Give the extent of all Plasmodium falciparum-infected red blood cells.
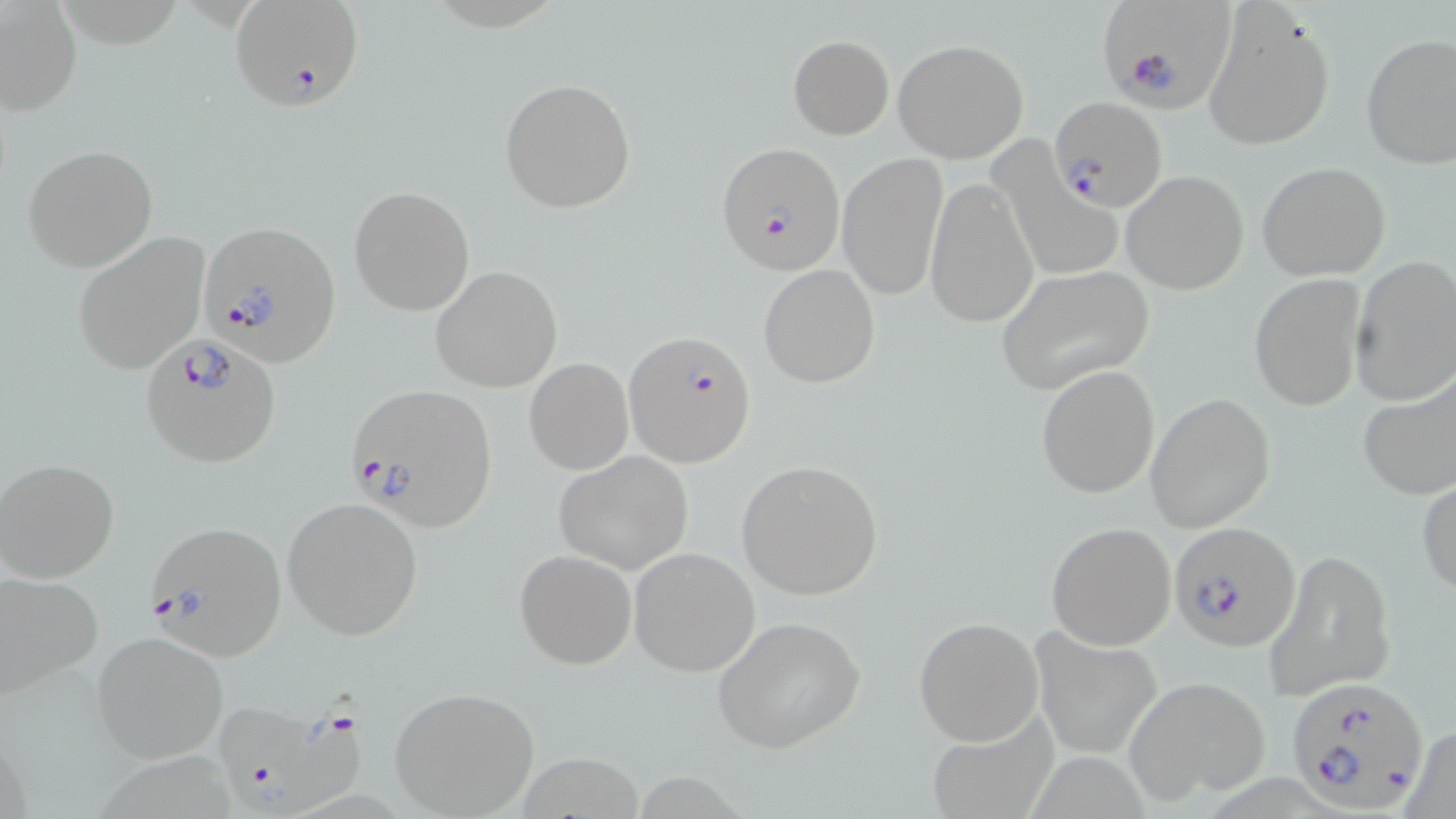
Approximate bounding boxes as (x1,y1)-(x2,y2) corner pairs in pixels.
Plasmodium falciparum-infected red blood cells: (228,1)-(364,113), (1099,2)-(1237,114), (1050,97)-(1166,212), (716,142)-(846,276), (193,229)-(336,362), (625,328)-(757,468), (140,333)-(282,467), (344,382)-(499,533), (141,521)-(285,658), (1168,521)-(1300,653), (1286,677)-(1430,814), (212,692)-(374,818).

{
  "slide_level_diagnosis": "Plasmodium falciparum",
  "preparation": "thin blood film",
  "image_size": "1456×819 pixels",
  "uninfected_red_blood_cell_locations": "approximate bounding boxes as (x1,y1)-(x2,y2) corner pairs in pixels: (1,2)-(81,115), (1200,3)-(1336,152), (1359,33)-(1456,169), (788,35)-(893,140), (892,38)-(1028,163), (500,78)-(637,215), (988,141)-(1124,286), (23,144)-(158,271), (837,152)-(947,300), (1258,163)-(1390,281), (1122,170)-(1249,295), (923,176)-(1038,329), (348,186)-(475,314), (71,233)-(208,372), (1348,256)-(1456,406), (757,264)-(880,388), (430,265)-(564,392), (995,265)-(1154,396), (1249,273)-(1365,413), (523,357)-(635,475), (1036,365)-(1159,499), (1357,372)-(1456,501), (1145,392)-(1276,533), (553,450)-(697,575), (0,458)-(120,584), (736,460)-(884,600), (1416,475)-(1456,597), (281,496)-(423,640), (1047,521)-(1177,649), (629,546)-(761,676), (514,549)-(637,668), (1268,549)-(1394,700), (0,572)-(103,701), (913,615)-(1043,744), (715,617)-(866,755), (1031,627)-(1165,759), (91,630)-(230,762), (1124,674)-(1271,807), (388,685)-(540,817), (922,711)-(1059,819), (1395,725)-(1456,819)",
  "magnification": "1000x",
  "modality": "light microscopy",
  "stain": "May-Grünwald-Giemsa",
  "field_of_view": "one of a larger specimen"
}